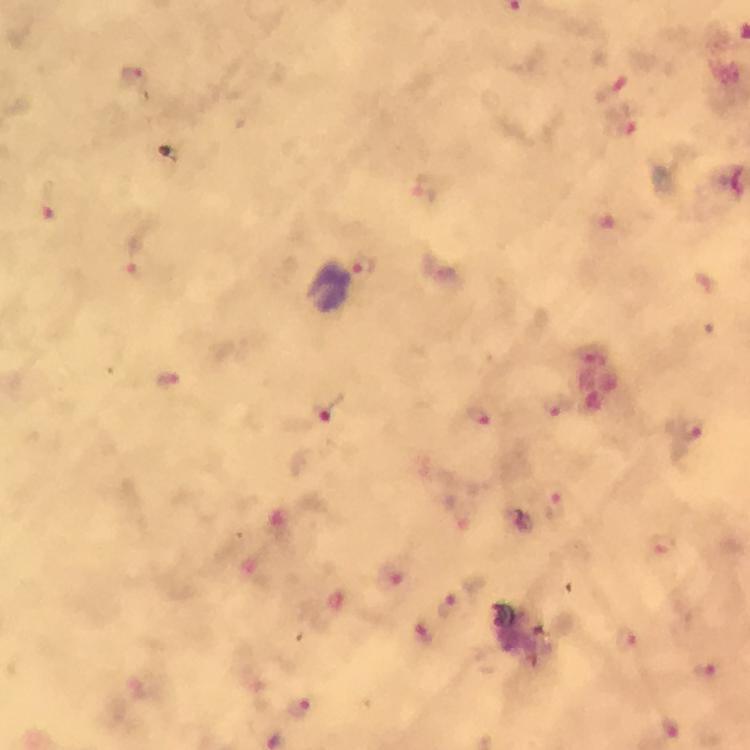

image size = 750×750 pixels
stain = Giemsa
magnification = 100x
cropped from = a single field of view
capture = smartphone photograph through a microscope
preparation = thick blood smear
context = from a diagnostic examination for malaria
immersion oil = applied
malaria parasite locations = approximate centers as {x, y} in pixels: {132, 78}, {616, 85}, {48, 204}, {365, 267}, {556, 403}, {331, 411}, {480, 416}, {689, 430}, {555, 506}, {391, 576}, {451, 604}, {424, 633}, {627, 638}, {704, 667}, {300, 708}, {670, 730}